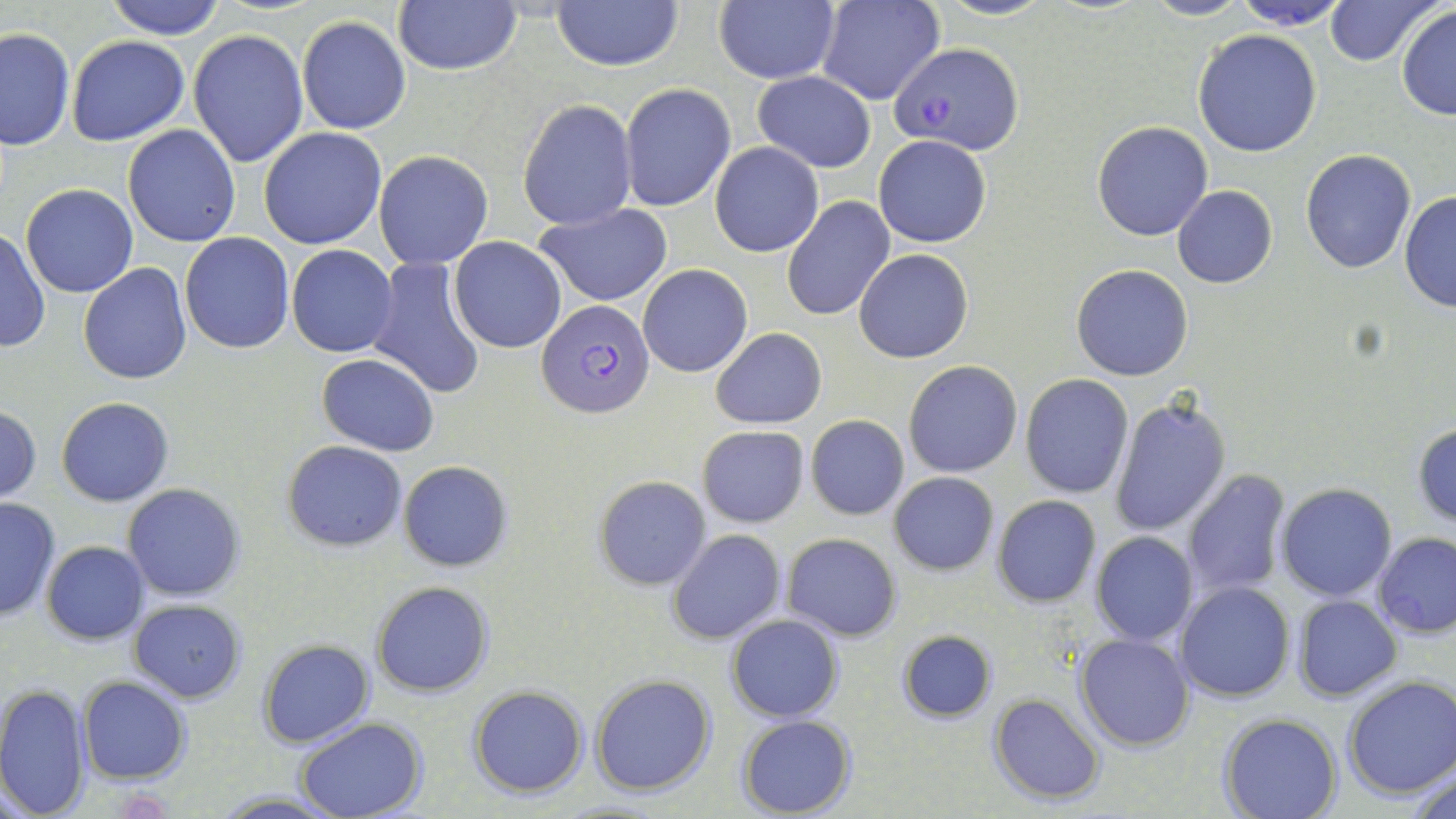

Summary:
  - Coordinate format: approximate bounding boxes as [x1, y1, x2, y2] in pixels
  - Uninfected red blood cell locations: [104, 0, 227, 40], [936, 0, 1055, 21], [1140, 0, 1254, 21], [1230, 0, 1353, 30], [1323, 0, 1441, 66], [550, 1, 683, 70], [815, 1, 944, 105], [393, 2, 521, 77], [713, 2, 839, 85], [1396, 6, 1456, 122], [296, 15, 411, 135], [0, 27, 73, 151], [1193, 28, 1322, 157], [189, 29, 308, 166], [66, 35, 191, 146], [753, 70, 875, 172], [620, 84, 735, 212], [517, 98, 636, 232], [1091, 120, 1214, 241], [122, 124, 242, 248], [258, 126, 387, 249], [874, 135, 990, 247], [711, 143, 824, 257], [1300, 149, 1417, 274], [374, 151, 493, 270], [21, 185, 139, 297], [1172, 185, 1277, 287], [1399, 191, 1456, 312], [783, 195, 896, 322], [534, 204, 672, 306], [0, 228, 49, 354], [180, 232, 295, 354], [448, 237, 568, 354], [287, 244, 397, 356], [855, 248, 973, 363], [367, 257, 489, 400], [79, 263, 192, 384], [638, 264, 752, 378], [1072, 264, 1193, 381], [710, 327, 827, 430], [316, 354, 439, 455], [903, 360, 1023, 478], [1020, 374, 1135, 498], [1108, 395, 1230, 537], [56, 396, 174, 507], [0, 407, 42, 502], [806, 414, 909, 520], [1413, 422, 1456, 527], [696, 426, 810, 528], [283, 440, 408, 551], [397, 461, 513, 571], [1181, 469, 1292, 600], [889, 471, 999, 575], [592, 475, 711, 589], [1278, 483, 1398, 601], [123, 484, 245, 600], [886, 486, 1103, 597], [0, 496, 62, 622], [992, 496, 1101, 607], [668, 529, 784, 645], [782, 532, 902, 641], [1090, 532, 1197, 645], [1373, 532, 1456, 638], [42, 540, 150, 644], [370, 581, 494, 698], [1174, 582, 1293, 702], [1293, 595, 1401, 700], [129, 599, 247, 702], [726, 613, 844, 721], [896, 628, 997, 723], [1075, 632, 1195, 750], [258, 640, 374, 748], [589, 672, 717, 796], [76, 674, 191, 785], [1342, 674, 1456, 800], [0, 682, 90, 819], [468, 684, 588, 797], [990, 693, 1106, 805], [1219, 712, 1342, 818], [735, 715, 856, 819], [296, 718, 426, 819], [1408, 763, 1456, 819], [210, 790, 347, 818]
  - Plasmodium falciparum-infected red blood cell locations: [890, 43, 1024, 153], [538, 301, 655, 420]
  - Slide-level diagnosis: Plasmodium falciparum
  - Stain: May-Grünwald-Giemsa
  - Field of view: single
  - Modality: light microscopy
  - Magnification: 1000x
  - Image size: 1456×819 pixels
  - Preparation: thin blood film